Identify the cell.
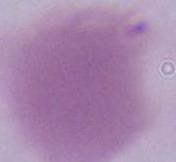
This is an erythrocyte.

Summary:
  - Magnification: 1000x
  - Modality: photomicrograph